Outline each Plasmodium falciparum-infected red blood cell.
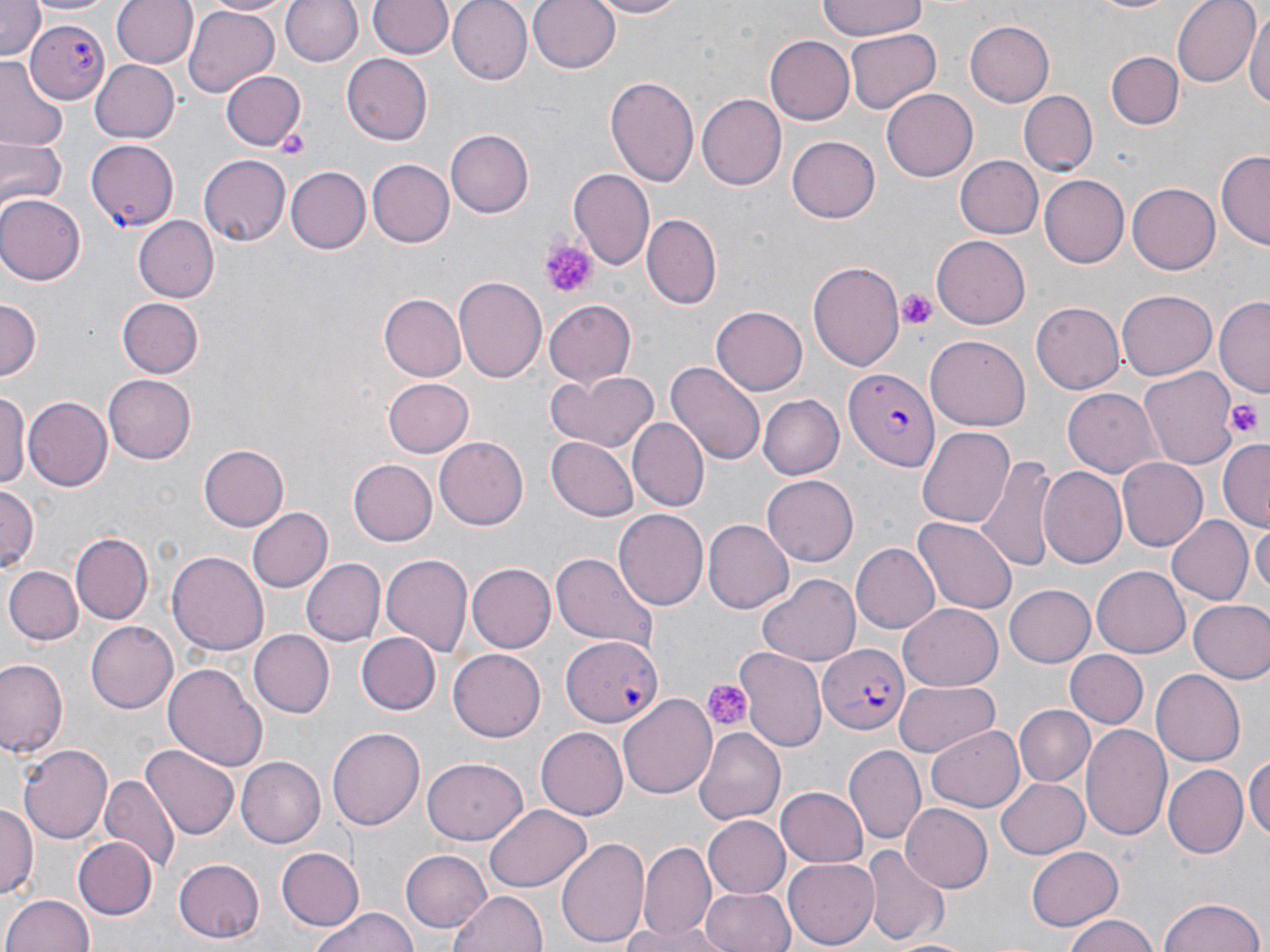
Approximate bounding boxes as (x1, y1, x2, y2) in pixels.
Plasmodium falciparum-infected red blood cells: (26, 20, 111, 104), (87, 140, 179, 232), (845, 365, 940, 474), (559, 636, 664, 729), (819, 645, 909, 733).

{
  "slide_level_diagnosis": "Plasmodium falciparum",
  "modality": "light microscopy",
  "image_size": "1270×952 pixels",
  "magnification": "1000x",
  "stain": "May-Grünwald-Giemsa",
  "preparation": "thin blood smear",
  "field_of_view": "single",
  "platelet_locations": "approximate bounding boxes as (x1, y1, x2, y2) in pixels: (542, 238, 596, 298), (898, 291, 937, 329), (1225, 397, 1264, 441), (699, 678, 752, 732)",
  "uninfected_red_blood_cell_locations": "approximate bounding boxes as (x1, y1, x2, y2) in pixels: (0, 0, 44, 62), (27, 0, 118, 18), (109, 0, 195, 70), (197, 0, 297, 17), (282, 0, 363, 67), (366, 0, 454, 59), (447, 0, 530, 83), (529, 0, 622, 75), (587, 0, 692, 19), (816, 0, 930, 40), (1172, 0, 1258, 87), (1078, 1, 1192, 17), (184, 5, 279, 97), (1246, 5, 1270, 120), (963, 17, 1054, 105), (845, 29, 940, 114), (765, 38, 854, 123), (1107, 51, 1184, 129), (343, 55, 433, 143), (0, 57, 68, 150), (89, 59, 180, 143), (220, 69, 304, 149), (605, 76, 700, 189), (880, 88, 977, 182), (1019, 91, 1098, 174), (695, 94, 784, 190), (444, 130, 531, 218), (0, 136, 65, 214), (788, 136, 880, 223), (1218, 150, 1269, 251), (199, 154, 289, 248), (955, 154, 1044, 238), (367, 159, 455, 248), (285, 167, 368, 254), (568, 170, 655, 271), (1040, 175, 1128, 267), (1128, 181, 1223, 273), (0, 194, 85, 286), (643, 213, 719, 309), (136, 215, 218, 302), (930, 235, 1030, 329), (806, 261, 906, 372), (454, 275, 548, 385), (1118, 288, 1216, 377), (380, 293, 466, 379), (0, 298, 40, 380), (118, 298, 203, 378), (1215, 298, 1269, 396), (543, 299, 639, 386), (1030, 300, 1124, 396), (711, 305, 806, 394), (926, 334, 1028, 427), (665, 361, 765, 466), (1140, 365, 1239, 470), (545, 369, 660, 454), (103, 374, 195, 463), (381, 378, 473, 458), (1063, 386, 1161, 476), (0, 387, 30, 495), (757, 395, 843, 480), (24, 397, 112, 491), (631, 419, 706, 510), (918, 425, 1016, 527), (547, 437, 638, 521), (437, 438, 527, 529), (1219, 439, 1269, 531), (198, 444, 290, 532), (1117, 457, 1207, 551), (977, 458, 1056, 573), (346, 460, 436, 546), (1040, 467, 1127, 569), (763, 477, 857, 563), (0, 485, 39, 571), (247, 506, 333, 593), (613, 510, 707, 611), (915, 515, 1018, 614), (1167, 515, 1252, 606), (704, 519, 793, 614), (1252, 519, 1269, 603), (73, 532, 153, 623), (851, 543, 940, 633), (167, 549, 268, 652), (381, 553, 473, 658), (550, 553, 659, 652), (300, 558, 384, 647), (467, 563, 557, 653), (1091, 565, 1190, 658), (6, 567, 80, 645), (758, 574, 861, 666), (1003, 583, 1095, 668), (1188, 599, 1270, 684), (899, 603, 1003, 689), (86, 621, 178, 713), (248, 630, 336, 718), (358, 632, 439, 714), (448, 649, 546, 741), (736, 649, 826, 752), (1066, 649, 1147, 729), (1, 659, 65, 758), (162, 660, 267, 770), (1152, 669, 1246, 767), (895, 680, 1000, 758), (618, 694, 717, 800), (1015, 703, 1094, 783), (1081, 723, 1171, 839), (926, 725, 1024, 812), (326, 727, 426, 832), (694, 727, 784, 824), (534, 728, 627, 821), (18, 741, 112, 845), (142, 742, 238, 840), (842, 744, 924, 844), (1246, 754, 1270, 846), (235, 756, 325, 848), (421, 759, 529, 846), (1163, 764, 1247, 858), (100, 775, 177, 871), (995, 775, 1089, 857), (776, 786, 867, 867), (0, 802, 36, 899), (900, 804, 993, 893), (483, 805, 591, 891), (703, 815, 791, 899), (557, 837, 653, 948), (75, 838, 156, 918), (640, 843, 715, 937), (1025, 845, 1123, 931), (862, 847, 947, 945), (278, 848, 363, 930), (402, 849, 491, 933), (784, 855, 880, 946), (172, 857, 265, 941), (703, 885, 794, 952), (446, 887, 548, 952), (3, 893, 95, 952), (1160, 896, 1265, 952), (315, 909, 419, 952), (1060, 915, 1161, 952), (615, 924, 733, 951)"
}